Give the position of every P. falciparum parasite, noting its life-cycle stage.
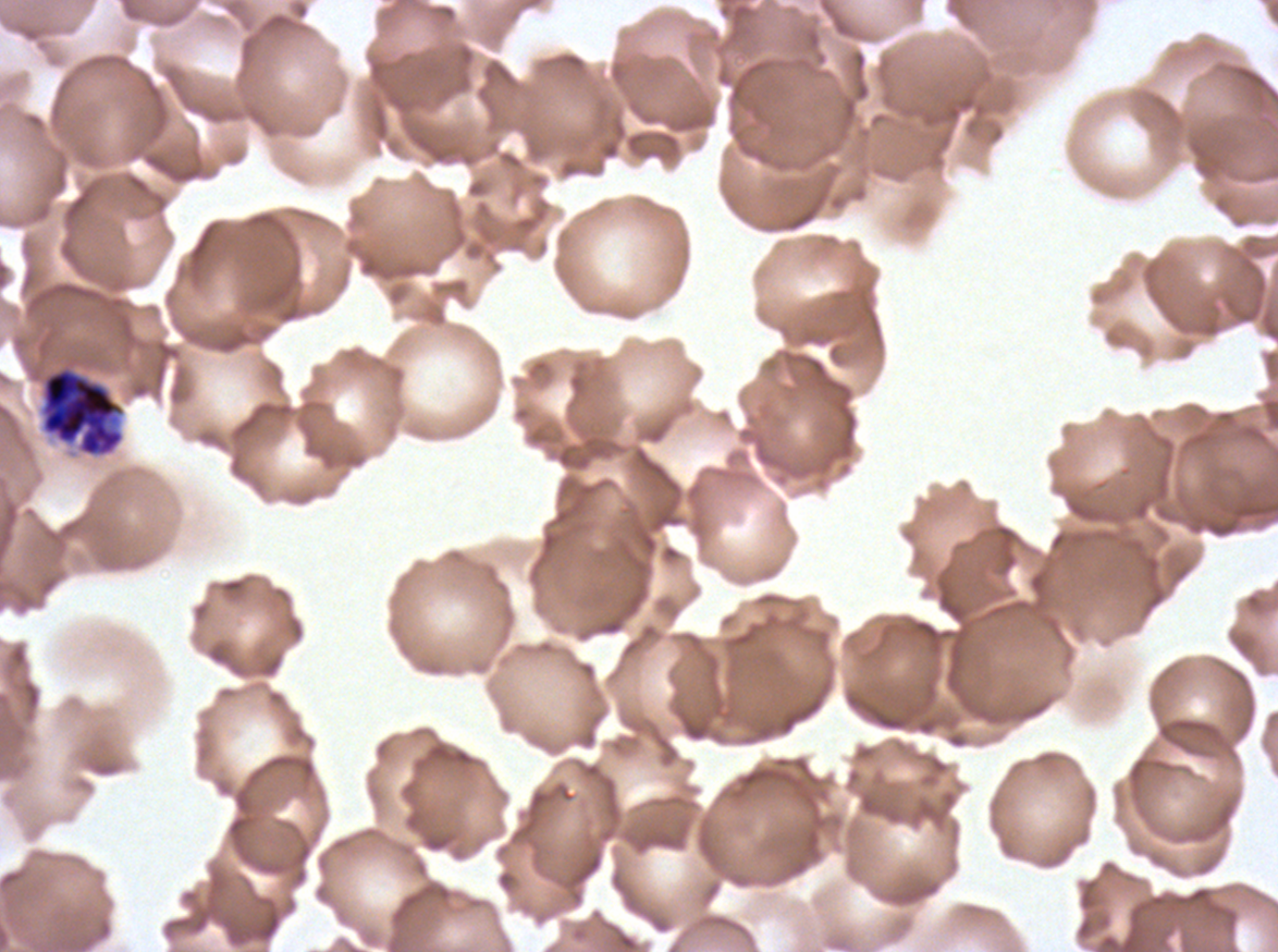
Approximate bounding boxes as {x1, y1, x2, y2} in pixels.
Early schizonts: {40, 366, 125, 458}.
No rings, late-ring/early-trophozoite forms, mid trophozoites, late trophozoites, late schizonts, segmenters, or gametocytes observed.

A sub-image separated from a larger composite. Giemsa-stained preparation. Thin blood film. Image is 1278×952 pixels. P. falciparum cultured ex vivo for 24 to 48 hours, from a patient in The Gambia.